Evaluate for malaria.
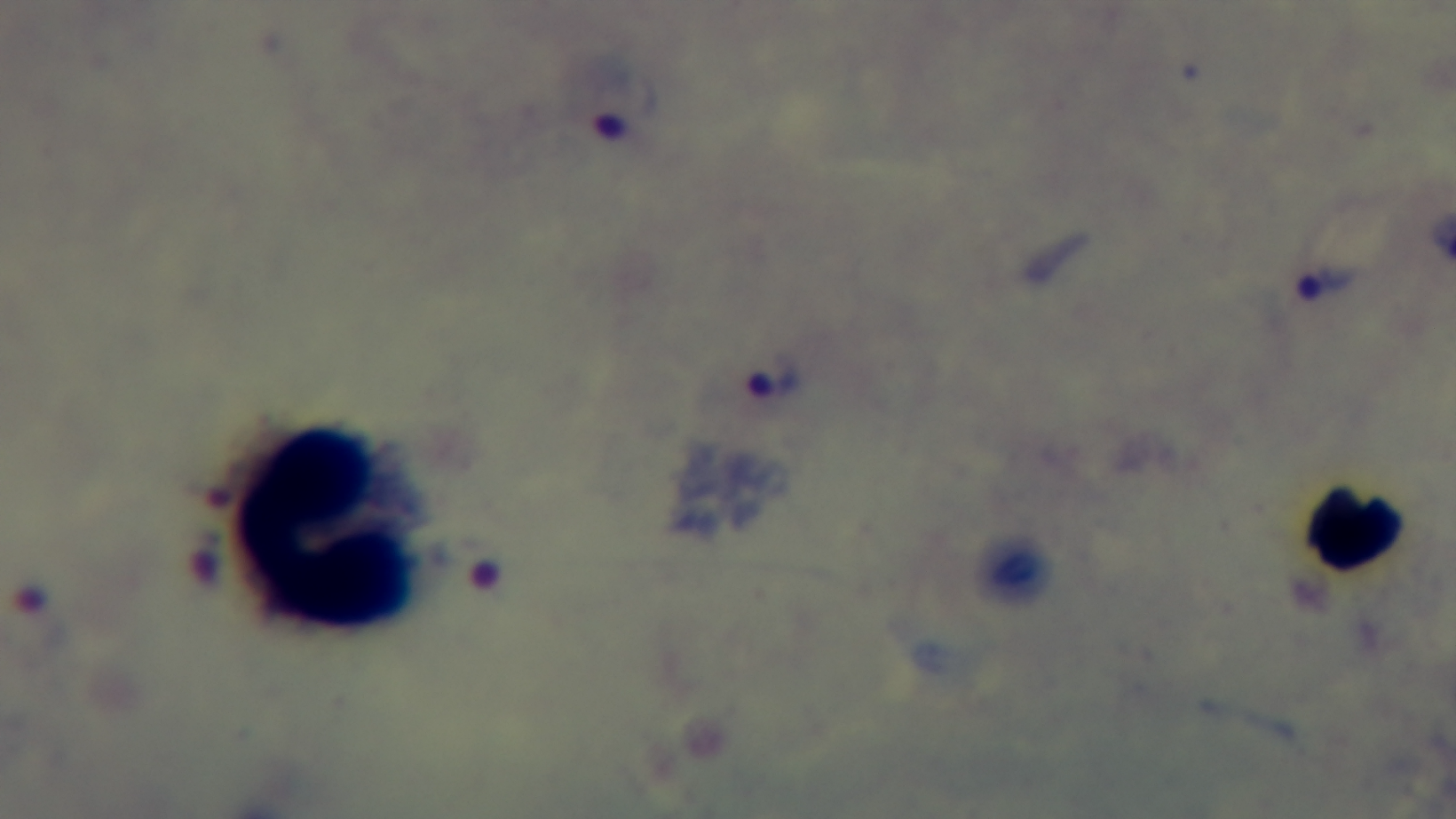
It is infected.

Summary:
  - Objective: 100x oil immersion
  - Preparation: thick blood film
  - Capture: mounted 4K digital camera
  - Field of view: single
  - Modality: light microscopy
  - Stain: Giemsa